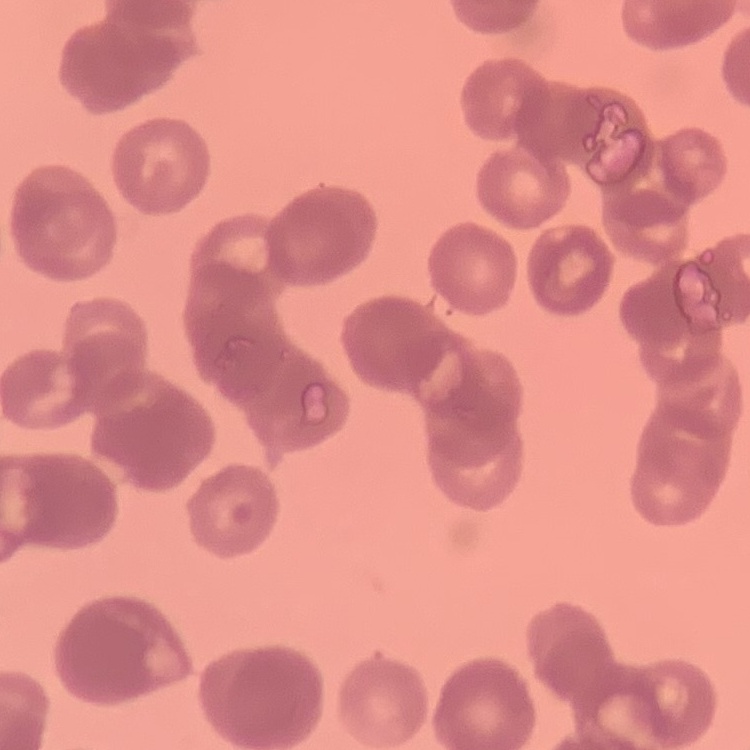
Summary:
  - Red blood cell morphology: rouleaux formation
  - Stain: Field's or Giemsa
  - Preparation: thin blood smear
  - Image type: one tile cut from a larger photomicrograph